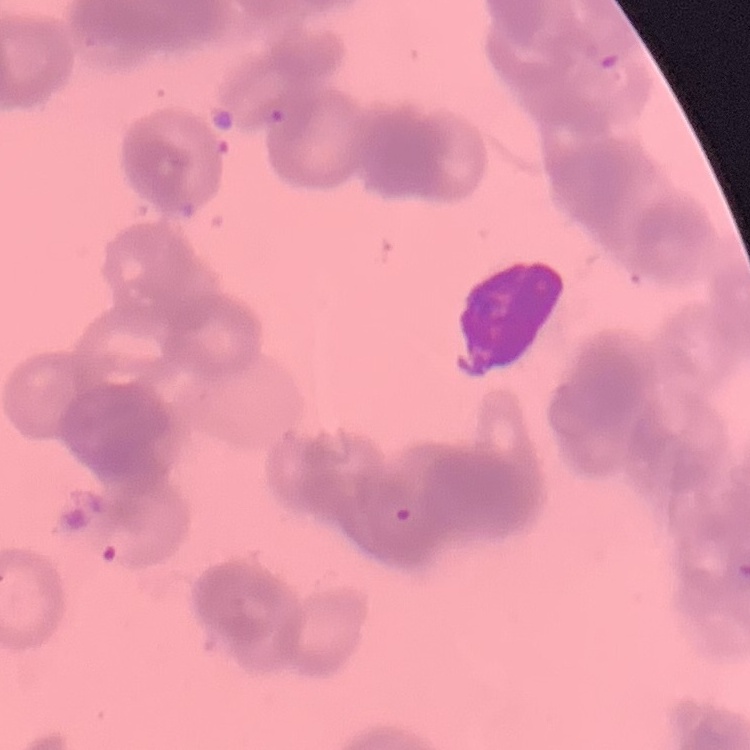

red blood cell morphology = rouleaux formation
preparation = thin blood smear
image type = square crop of a larger photomicrograph
stain = Field's or Giemsa